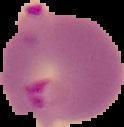

Summary:
  - Result: Plasmodium parasites detected
  - Preparation: thin blood smear
  - Image size: 124×127 pixels
  - Image type: segmented cell region on a black background